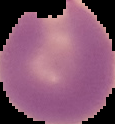

{
  "preparation": "thin blood smear",
  "result": "Plasmodium parasites detected",
  "image_size": "115×124 pixels",
  "image_type": "segmented cell region on a black background"
}